Describe the morphology of the red blood cells.
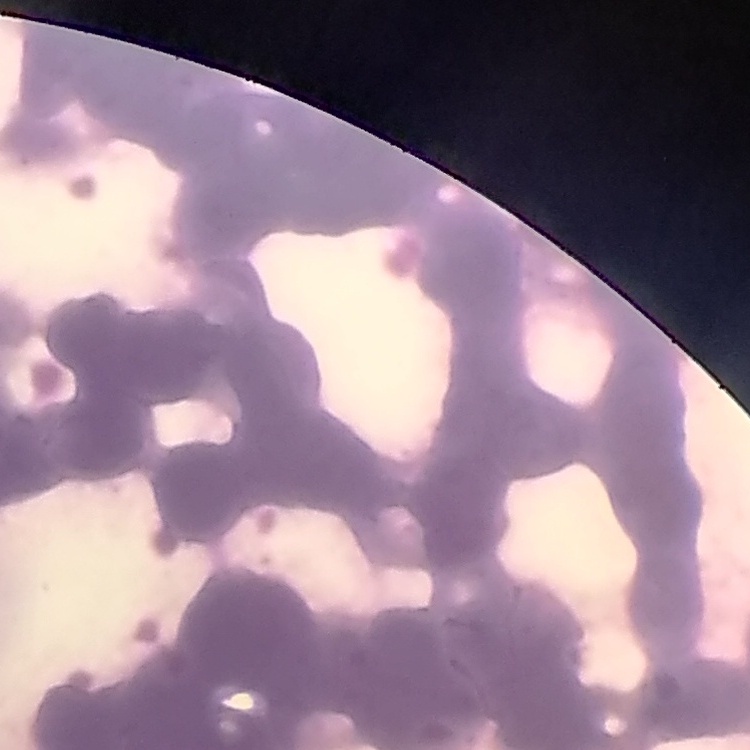

They show rouleaux formation.

stain = Field's or Giemsa
image type = one tile cut from a larger photomicrograph
preparation = thin peripheral smear